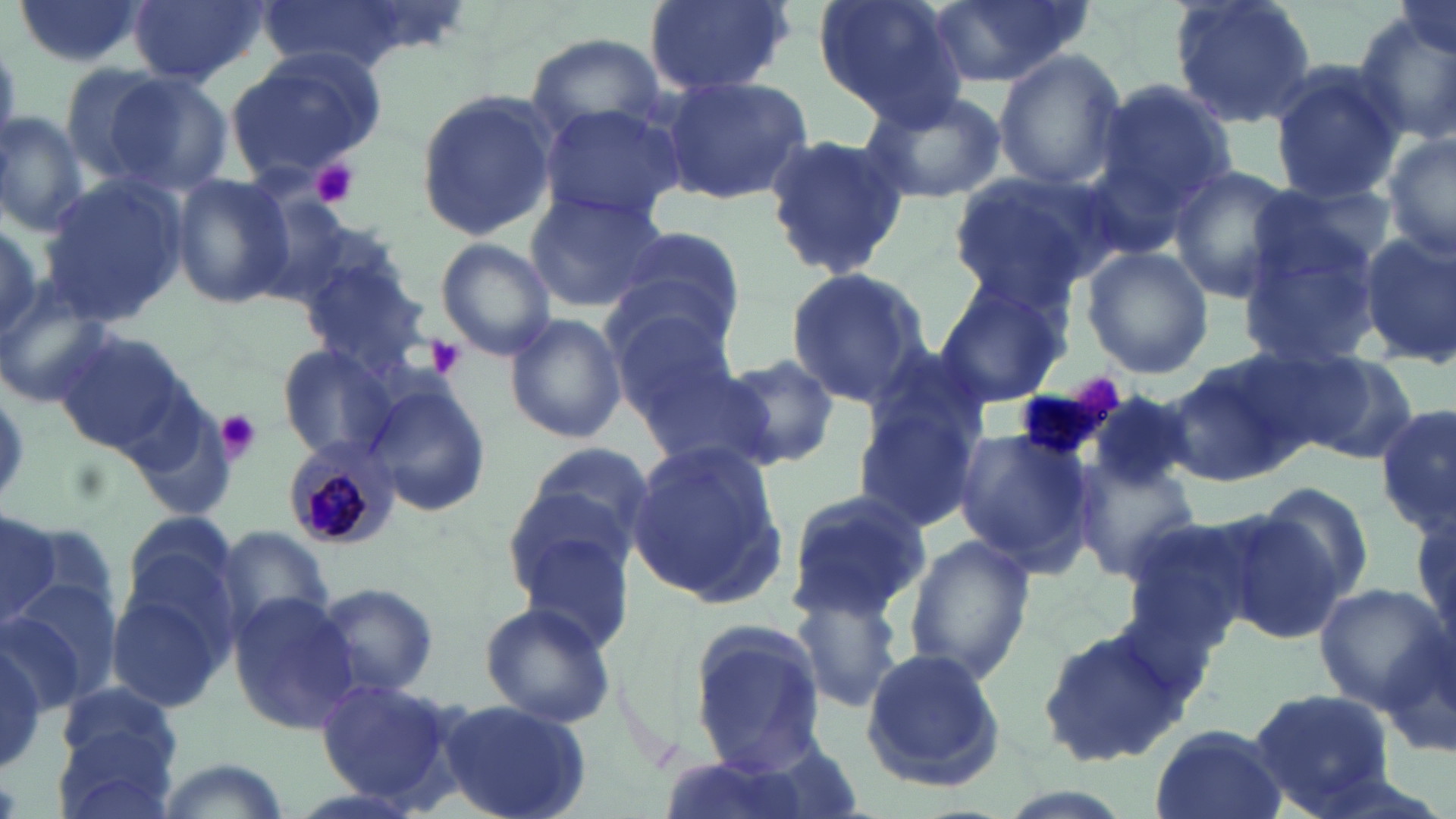

slide_level_diagnosis: Plasmodium malariae
magnification: 1000x
modality: light microscopy
uninfected_red_blood_cell_locations: 'approximate bounding boxes as (x1, y1, x2, y2) in pixels: (10, 0, 146, 69), (127, 0, 268, 87), (258, 0, 414, 75), (638, 0, 797, 97), (813, 0, 966, 125), (925, 0, 1092, 87), (1169, 0, 1317, 129), (1350, 6, 1456, 147), (526, 31, 668, 143), (224, 46, 389, 181), (991, 50, 1128, 192), (57, 64, 173, 181), (1268, 64, 1404, 202), (96, 68, 234, 193), (1088, 74, 1241, 242), (658, 76, 813, 207), (856, 87, 1006, 202), (412, 88, 559, 242), (538, 101, 686, 226), (0, 110, 90, 238), (761, 131, 912, 277), (1383, 132, 1456, 266), (1165, 164, 1299, 303), (169, 173, 296, 309), (946, 173, 1117, 307), (37, 175, 190, 325), (1249, 183, 1392, 299), (522, 189, 668, 312), (253, 198, 390, 310), (0, 214, 51, 342), (615, 220, 749, 343), (1358, 230, 1456, 365), (435, 238, 556, 359), (1080, 246, 1213, 379), (1235, 246, 1386, 371), (300, 256, 433, 378), (784, 266, 928, 407), (934, 279, 1067, 410), (0, 285, 118, 409), (605, 295, 738, 416), (505, 315, 627, 445), (58, 329, 185, 454), (857, 340, 993, 455), (275, 343, 406, 464), (1160, 351, 1313, 485), (1291, 352, 1422, 465), (723, 354, 842, 468), (632, 363, 778, 470), (367, 382, 490, 519), (1087, 389, 1197, 496), (848, 400, 986, 536), (1377, 402, 1455, 536), (952, 427, 1097, 572), (518, 438, 656, 556), (625, 440, 786, 608), (1076, 452, 1216, 598), (498, 476, 641, 603), (1256, 480, 1376, 611), (784, 488, 932, 620), (0, 505, 58, 631), (1216, 505, 1357, 644), (116, 511, 246, 639), (1412, 511, 1455, 656), (212, 528, 333, 632), (518, 532, 634, 651), (905, 534, 1037, 685), (314, 582, 439, 697), (793, 582, 905, 714), (4, 583, 116, 709), (1313, 583, 1450, 713), (227, 590, 363, 731), (110, 592, 231, 712), (478, 603, 617, 731), (684, 616, 831, 778), (1034, 627, 1190, 766), (1380, 627, 1456, 763), (0, 634, 55, 776), (863, 649, 1008, 791), (316, 679, 458, 804), (56, 682, 180, 771), (1247, 687, 1394, 817), (437, 699, 592, 819), (1149, 725, 1288, 819), (54, 731, 180, 819), (150, 756, 297, 819)'
field_of_view: single
stain: May-Grünwald-Giemsa
image_size: 1456×819 pixels
preparation: thin blood film
platelet_locations: 'approximate bounding boxes as (x1, y1, x2, y2) in pixels: (312, 161, 358, 208), (425, 338, 466, 378), (212, 408, 264, 464)'
plasmodium_malariae_infected_red_blood_cell_locations: 'approximate bounding boxes as (x1, y1, x2, y2) in pixels: (283, 439, 395, 549)'